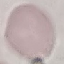

Result: no malaria parasites detected. Photographed with a smartphone camera at the microscope eyepiece. Cell patch, automatically extracted from a larger field of view and resized to 64 × 64 pixels. Thin blood film. Giemsa-stained preparation.